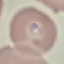

Summary:
  - Malaria status: parasitized
  - Image type: cell patch, automatically extracted from a larger field of view and resized to 64 × 64 pixels
  - Preparation: thin blood smear
  - Capture: smartphone through the microscope eyepiece
  - Stain: Giemsa